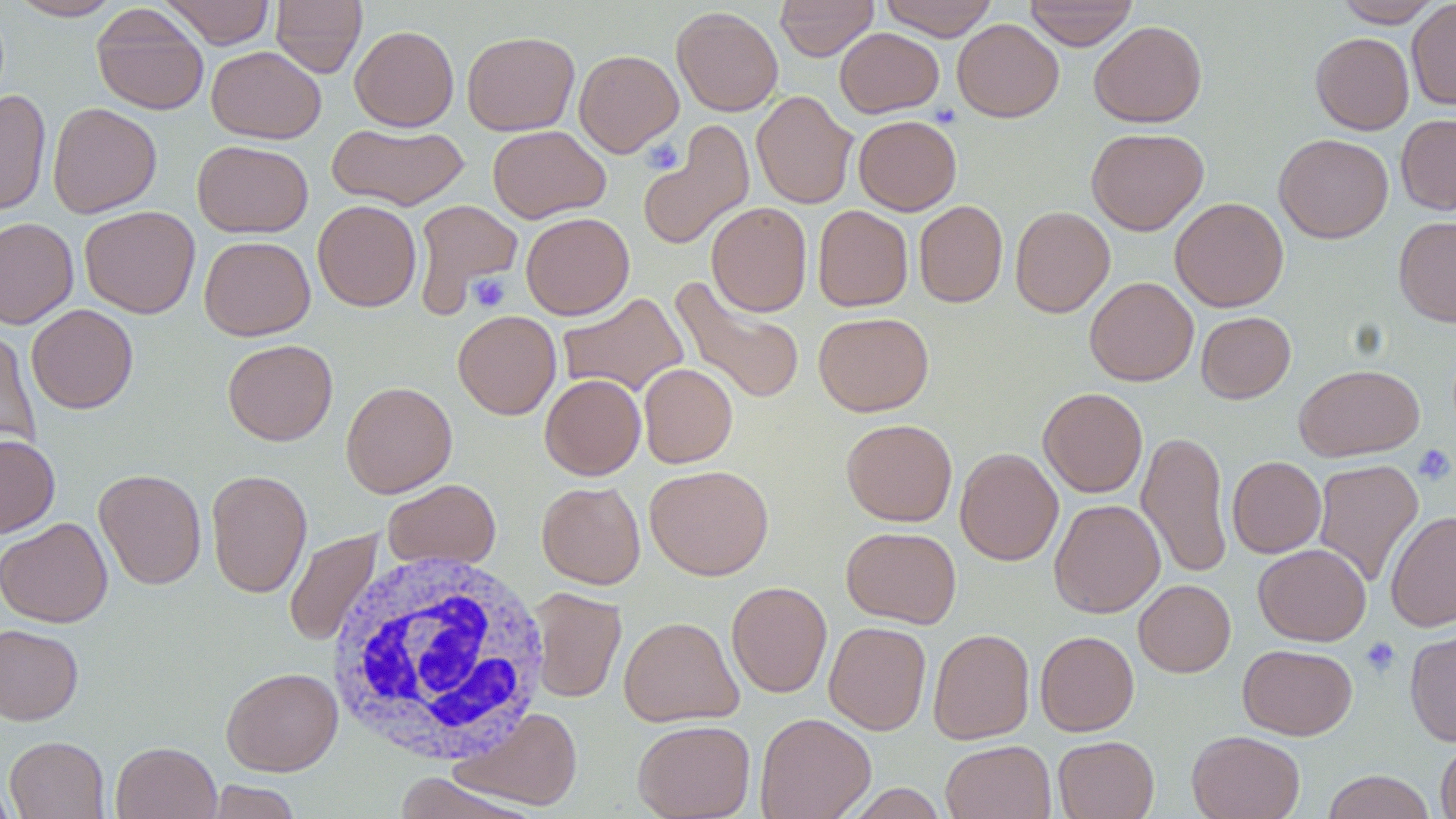

Approximate bounding boxes as (x1,y1)-(x2,y2) corner pairs in pixels. Uninfected red blood cell locations: (7,0)-(123,21), (160,0)-(275,48), (270,0)-(367,78), (774,0)-(879,61), (878,0)-(999,40), (1024,0)-(1138,50), (1334,0)-(1443,27), (1406,0)-(1456,109), (92,5)-(209,115), (671,5)-(784,116), (952,19)-(1064,122), (1089,20)-(1207,128), (350,25)-(459,131), (834,27)-(944,117), (462,31)-(580,135), (1311,32)-(1414,135), (206,46)-(325,143), (574,49)-(683,157), (0,89)-(51,216), (751,90)-(858,209), (47,102)-(162,218), (1396,113)-(1456,215), (853,115)-(961,215), (640,121)-(754,252), (327,122)-(469,210), (487,125)-(610,223), (1086,127)-(1208,235), (1274,133)-(1393,243), (192,140)-(313,237), (1170,197)-(1289,312), (411,198)-(523,316), (312,200)-(422,312), (913,200)-(1008,308), (706,202)-(812,317), (812,205)-(913,312), (79,206)-(200,318), (1010,206)-(1115,317), (520,212)-(634,320), (1394,216)-(1456,326), (0,217)-(79,330), (199,236)-(315,341), (670,276)-(806,406), (1085,277)-(1198,386), (557,292)-(688,397), (27,304)-(138,414), (453,310)-(561,419), (1196,311)-(1295,403), (814,312)-(933,416), (0,327)-(40,453), (223,339)-(338,446), (639,363)-(738,468), (1294,364)-(1425,461), (540,374)-(646,480), (341,380)-(457,498), (1038,387)-(1147,497), (841,419)-(957,526), (1137,430)-(1233,579), (0,434)-(60,538), (955,447)-(1063,565), (1227,456)-(1326,558), (1313,459)-(1424,587), (644,464)-(773,580), (94,468)-(207,590), (206,468)-(312,598), (382,479)-(501,571), (536,481)-(645,589), (1049,499)-(1165,617), (1386,510)-(1456,632), (0,517)-(112,627), (841,526)-(961,628), (284,528)-(383,647), (1253,543)-(1371,646), (1134,579)-(1235,677), (727,581)-(832,697), (527,588)-(627,703), (618,616)-(743,727), (824,621)-(931,735), (0,623)-(84,725), (1404,624)-(1456,746), (928,628)-(1034,744), (1035,631)-(1138,736), (1237,644)-(1357,740), (221,667)-(343,775), (453,707)-(583,811), (754,712)-(876,819), (633,719)-(755,819), (1187,730)-(1305,819), (4,735)-(110,818), (1053,735)-(1159,819), (1435,738)-(1456,819), (940,740)-(1056,819), (111,741)-(221,819), (1322,770)-(1436,819), (392,772)-(540,819), (0,774)-(17,819), (203,780)-(303,819). Platelet locations: (640,136)-(686,174), (467,273)-(511,313), (1412,443)-(1455,486), (1360,636)-(1401,678). White blood cell locations: (323,548)-(554,768). Slide-level diagnosis: negative for blood parasites. Light microscopy. Image is 1456×819 pixels. Thin blood smear. One field of a larger specimen. Captured at 1000x magnification. May-Grünwald-Giemsa stain.